Name the blood parasite species.
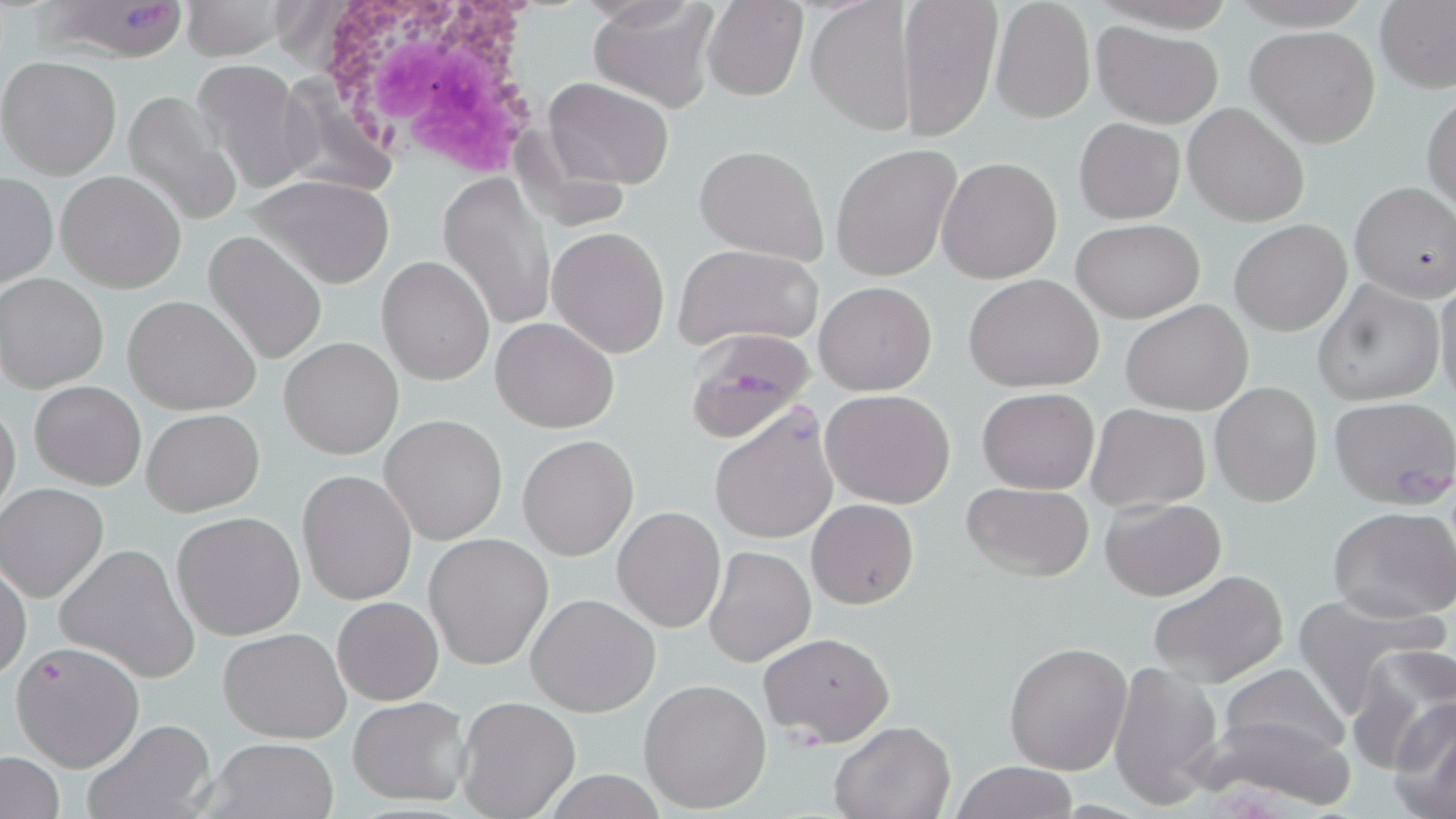

Plasmodium falciparum.

preparation = thin blood film
Plasmodium falciparum-infected red blood cell locations = approximate bounding boxes as named x1/y1/x2/y2 corners in pixels: (x1=33, y1=2, x2=193, y2=61), (x1=686, y1=332, x2=816, y2=440)
magnification = 1000x
modality = optical microscopy
stain = May-Grünwald-Giemsa
white blood cell locations = approximate bounding boxes as named x1/y1/x2/y2 corners in pixels: (x1=303, y1=0, x2=553, y2=179)
image size = 1456×819 pixels
uninfected red blood cell locations = approximate bounding boxes as named x1/y1/x2/y2 corners in pixels: (x1=179, y1=0, x2=292, y2=61), (x1=588, y1=0, x2=721, y2=112), (x1=899, y1=0, x2=1003, y2=140), (x1=703, y1=1, x2=806, y2=100), (x1=1375, y1=1, x2=1456, y2=94), (x1=807, y1=2, x2=918, y2=134), (x1=989, y1=3, x2=1093, y2=123), (x1=1091, y1=21, x2=1223, y2=128), (x1=1246, y1=26, x2=1380, y2=148), (x1=0, y1=55, x2=122, y2=179), (x1=191, y1=57, x2=315, y2=194), (x1=543, y1=76, x2=675, y2=189), (x1=121, y1=92, x2=244, y2=228), (x1=1423, y1=92, x2=1455, y2=213), (x1=1182, y1=103, x2=1310, y2=227), (x1=1074, y1=117, x2=1185, y2=224), (x1=511, y1=123, x2=630, y2=233), (x1=694, y1=143, x2=831, y2=265), (x1=830, y1=143, x2=962, y2=281), (x1=935, y1=156, x2=1061, y2=285), (x1=56, y1=170, x2=185, y2=293), (x1=1, y1=173, x2=57, y2=291), (x1=249, y1=174, x2=397, y2=289), (x1=439, y1=175, x2=557, y2=332), (x1=1350, y1=181, x2=1456, y2=302), (x1=1071, y1=218, x2=1204, y2=322), (x1=1230, y1=219, x2=1351, y2=335), (x1=547, y1=226, x2=670, y2=358), (x1=203, y1=230, x2=327, y2=366), (x1=1088, y1=232, x2=1221, y2=390), (x1=672, y1=244, x2=823, y2=350), (x1=377, y1=255, x2=494, y2=385), (x1=962, y1=273, x2=1105, y2=392), (x1=1433, y1=273, x2=1456, y2=406), (x1=1, y1=274, x2=108, y2=392), (x1=814, y1=280, x2=937, y2=395), (x1=1312, y1=281, x2=1444, y2=405), (x1=122, y1=295, x2=260, y2=417), (x1=1121, y1=301, x2=1254, y2=415), (x1=490, y1=317, x2=620, y2=434), (x1=279, y1=337, x2=402, y2=459), (x1=30, y1=380, x2=145, y2=491), (x1=1210, y1=382, x2=1323, y2=507), (x1=975, y1=387, x2=1100, y2=494), (x1=820, y1=388, x2=955, y2=508), (x1=1328, y1=396, x2=1456, y2=508), (x1=0, y1=399, x2=21, y2=523), (x1=1086, y1=403, x2=1211, y2=513), (x1=708, y1=404, x2=838, y2=547), (x1=142, y1=408, x2=262, y2=516), (x1=380, y1=414, x2=509, y2=544), (x1=518, y1=435, x2=638, y2=560), (x1=297, y1=469, x2=418, y2=605), (x1=1, y1=482, x2=109, y2=601), (x1=962, y1=482, x2=1096, y2=580), (x1=1100, y1=498, x2=1225, y2=600), (x1=807, y1=500, x2=919, y2=608), (x1=612, y1=506, x2=726, y2=632), (x1=1328, y1=506, x2=1456, y2=624), (x1=172, y1=511, x2=305, y2=640), (x1=423, y1=532, x2=553, y2=670), (x1=55, y1=543, x2=201, y2=684), (x1=704, y1=545, x2=815, y2=666), (x1=0, y1=558, x2=31, y2=683), (x1=1147, y1=570, x2=1289, y2=687), (x1=1292, y1=592, x2=1447, y2=716), (x1=526, y1=593, x2=659, y2=716), (x1=332, y1=596, x2=442, y2=705), (x1=217, y1=627, x2=351, y2=743), (x1=758, y1=632, x2=894, y2=746), (x1=11, y1=639, x2=146, y2=771), (x1=1003, y1=641, x2=1131, y2=776), (x1=1348, y1=645, x2=1456, y2=772), (x1=1107, y1=660, x2=1224, y2=809), (x1=1218, y1=664, x2=1348, y2=761), (x1=640, y1=678, x2=771, y2=813), (x1=456, y1=695, x2=580, y2=818), (x1=346, y1=696, x2=473, y2=805), (x1=1390, y1=698, x2=1456, y2=817), (x1=1197, y1=705, x2=1359, y2=813), (x1=81, y1=718, x2=218, y2=819), (x1=829, y1=720, x2=954, y2=819), (x1=203, y1=736, x2=340, y2=819), (x1=1, y1=751, x2=65, y2=818), (x1=948, y1=761, x2=1082, y2=818)
field of view = one of a larger specimen